Classify this cell by malaria status.
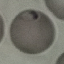
It is parasitized.

Giemsa-stained preparation. Thin blood film. Cell patch, automatically extracted from a larger field of view and resized to 64 × 64 pixels. Photographed with a smartphone camera at the microscope eyepiece.